Classify this cell by malaria status.
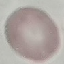
It is uninfected.

capture = smartphone through the microscope eyepiece
preparation = thin blood smear
stain = Giemsa
image type = cell patch, automatically extracted from a larger field of view and resized to 64 × 64 pixels